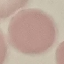
result = no malaria parasites seen
capture = smartphone through the microscope eyepiece
stain = Giemsa
image type = cell patch, automatically extracted from a larger field of view and resized to 64 × 64 pixels
preparation = thin blood smear